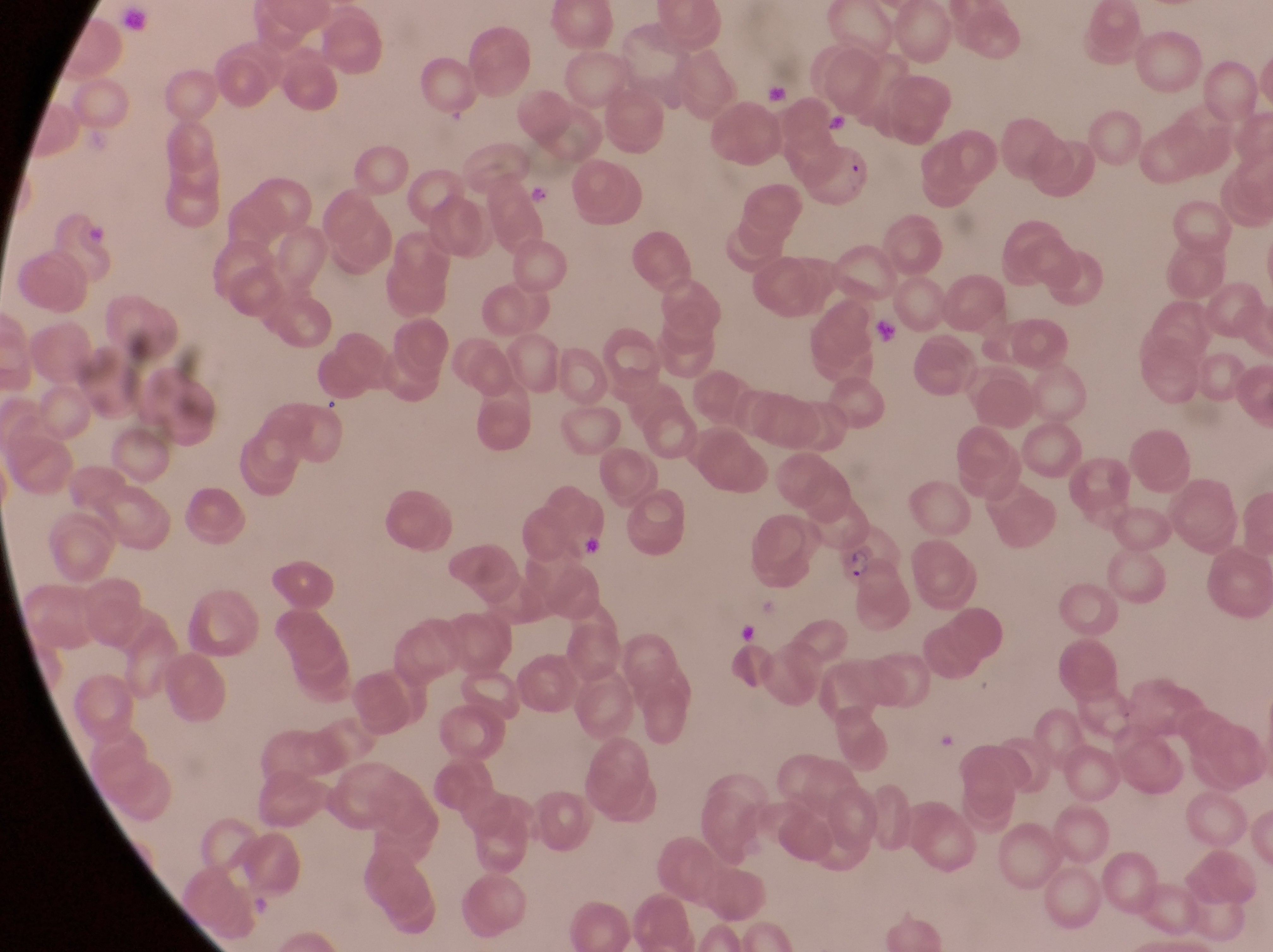 Approximate bounding boxes as {left, top, right, bottom} in pixels. Parasitised red blood cell locations: {834, 521, 906, 591}. Trophozoite locations: {524, 174, 561, 213}. Artifact (platelet-like body, stain precipitate, or debris) locations: {764, 85, 787, 105}, {827, 110, 851, 138}, {869, 307, 906, 359}, {318, 396, 349, 420}, {572, 522, 611, 562}, {735, 619, 759, 645}, {941, 732, 965, 753}. Collected in Uganda. Captured by a smartphone held over the eyepiece of an Olympus CX-23 microscope. Thin blood film. Single field of view. Image is 1273×952 pixels. At a magnification of 1000x.